Assess the morphology of the red blood cells.
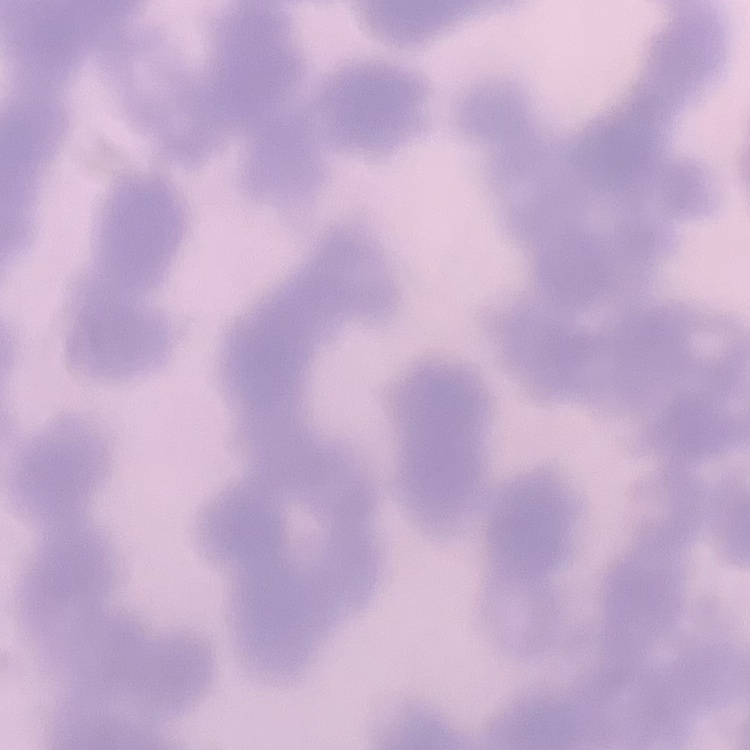

They show rouleaux formation.

Thin peripheral smear. Stained with either Field's or Giemsa. One tile cut from a larger photomicrograph.